Assess the morphology of the red blood cells.
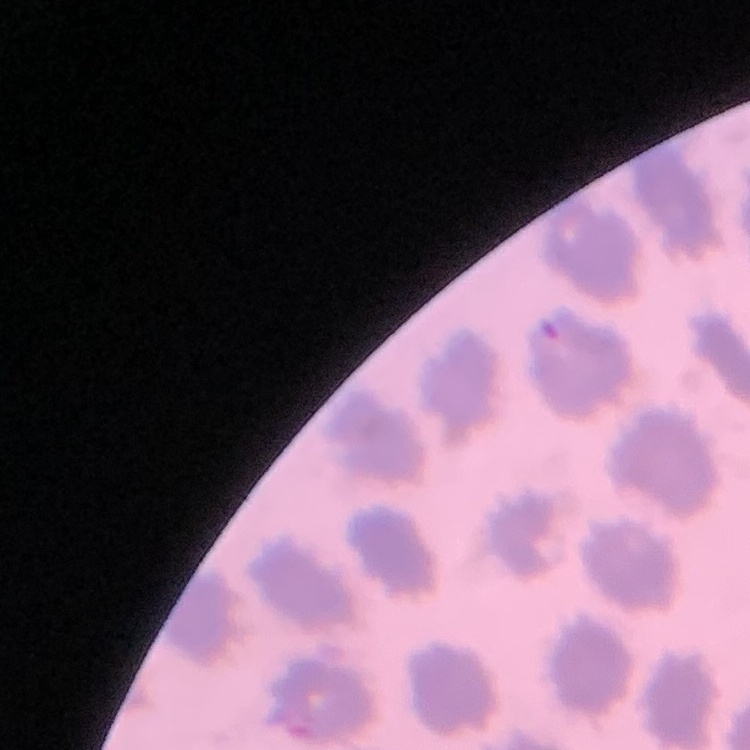
No rouleaux formation.

Thin blood smear. One tile cut from a larger photomicrograph. Stained with either Field's or Giemsa.